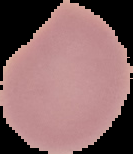
Summary:
  - Preparation: thin blood film
  - Result: no malaria parasites detected
  - Image size: 133×154 pixels
  - Image type: cell region segmented out of the field of view; surrounding area masked to black